Assess this cell for malaria.
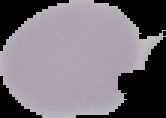
It is uninfected.

image size = 166×118 pixels
image type = cell region segmented out of the field of view; surrounding area masked to black
preparation = thin blood smear